State which parasite is depicted.
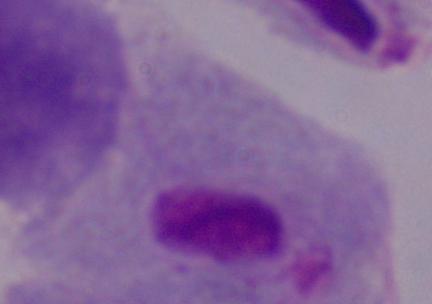
This is a trichomonad.

Micrograph. Captured at 1000x magnification.